Identify the parasite.
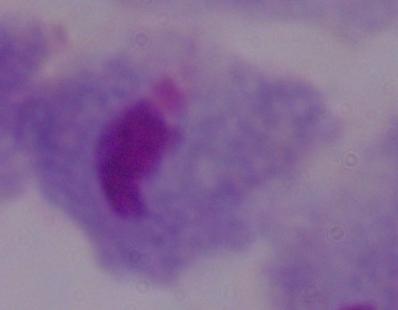

This is a trichomonad.

Captured at 1000x magnification. Photomicrograph.